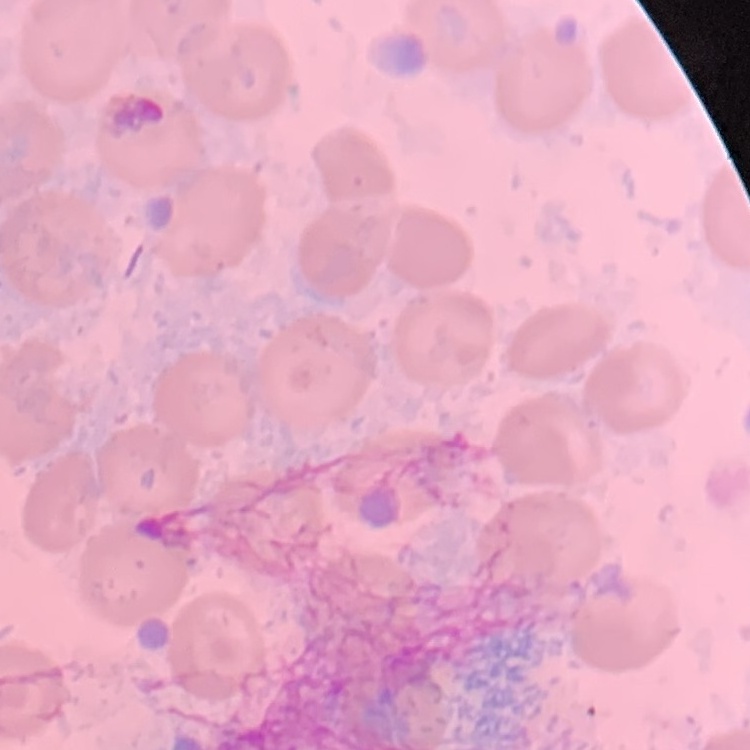

erythrocyte_morphology: no rouleaux formation
preparation: thin peripheral smear
image_type: square crop of a larger photomicrograph
stain: Field's or Giemsa